Assess this cell for malaria.
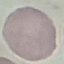

It is uninfected.

Cell patch, automatically extracted from a larger field of view and resized to 64 × 64 pixels. Giemsa stain. Thin smear of blood. Acquired by smartphone through the microscope eyepiece.